Assess this cell for malaria.
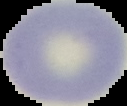
It is uninfected.

Cell region segmented out of the field of view; the surrounding area is masked to black. Image is 127×106 pixels. From a thin blood film.